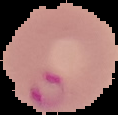

{
  "image_type": "cell region segmented out of the field of view; surrounding area masked to black",
  "result": "malaria parasites detected",
  "preparation": "thin blood smear",
  "image_size": "118×115 pixels"
}